Identify the blood parasite species.
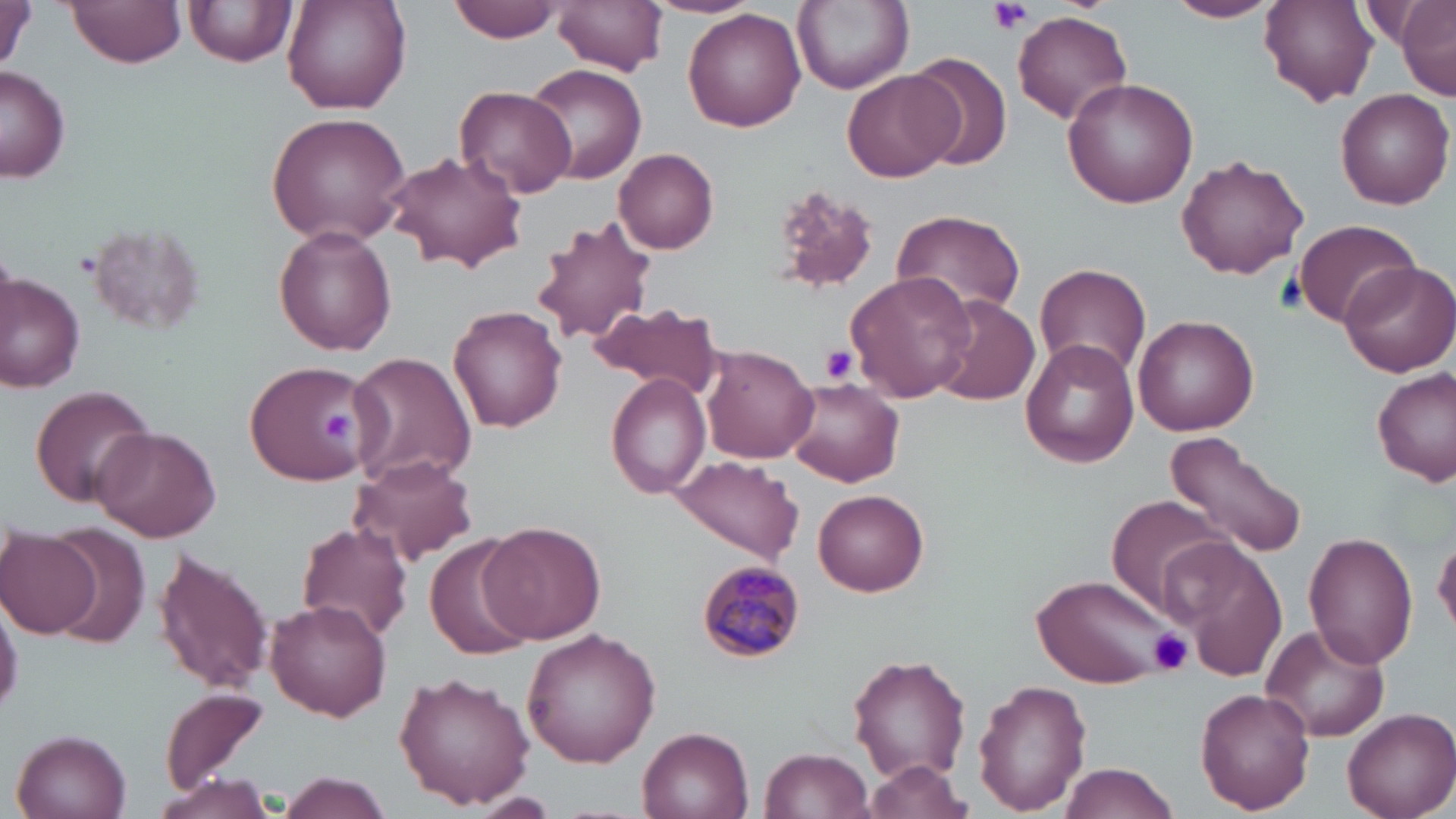
Plasmodium malariae.

Summary:
  - Coordinate format: approximate bounding boxes as (x1,y1)-(x2,y2) corner pairs in pixels
  - Platelet locations: (989,0)-(1033,34), (821,344)-(860,383), (322,409)-(357,442), (1148,627)-(1194,676)
  - Plasmodium malariae-infected red blood cell locations: (697,561)-(804,662)
  - Uninfected red blood cell locations: (0,0)-(35,76), (66,0)-(186,69), (186,0)-(297,69), (448,0)-(562,43), (553,0)-(668,75), (793,0)-(914,94), (1165,0)-(1282,23), (1258,0)-(1378,106), (282,1)-(412,115), (1395,1)-(1455,100), (680,6)-(804,134), (1013,12)-(1132,125), (906,52)-(1014,172), (523,62)-(645,185), (2,66)-(72,184), (842,69)-(960,183), (1062,77)-(1202,208), (456,85)-(577,199), (1334,90)-(1453,210), (267,111)-(412,248), (613,148)-(719,251), (383,150)-(527,275), (1176,155)-(1309,281), (767,183)-(880,297), (889,209)-(1027,317), (532,215)-(658,345), (1293,218)-(1422,331), (85,220)-(207,337), (274,226)-(397,356), (1338,261)-(1456,377), (1036,262)-(1152,379), (0,274)-(86,393), (845,274)-(971,403), (933,295)-(1040,405), (587,302)-(726,401), (448,304)-(568,433), (1132,315)-(1259,437), (1020,338)-(1139,466), (700,344)-(818,463), (349,352)-(477,491), (245,359)-(367,484), (1373,366)-(1455,486), (607,373)-(711,497), (783,378)-(904,487), (29,385)-(156,508), (93,427)-(221,542), (1163,432)-(1308,560), (349,453)-(478,567), (669,453)-(803,565), (814,489)-(928,597), (1107,499)-(1236,620), (294,520)-(412,644), (478,520)-(604,644), (42,527)-(147,645), (1302,530)-(1417,669), (2,531)-(102,637), (1169,533)-(1286,679), (1434,534)-(1456,634), (425,535)-(538,660), (153,545)-(274,697), (1035,575)-(1173,689), (0,584)-(21,723), (264,599)-(391,721), (1262,624)-(1390,742), (520,625)-(663,767), (849,655)-(971,781), (394,670)-(535,809), (974,681)-(1092,813), (158,686)-(272,796), (1195,687)-(1315,814), (1341,707)-(1454,819), (636,726)-(755,819), (11,729)-(134,819), (760,747)-(874,819), (864,759)-(975,817), (1058,764)-(1177,819), (156,772)-(274,819), (280,773)-(392,819), (480,793)-(554,816)
  - Modality: light microscopy
  - Magnification: 1000x
  - Field of view: single
  - Stain: May-Grünwald-Giemsa
  - Image size: 1456×819 pixels
  - Preparation: thin blood smear